Classify this cell by malaria status.
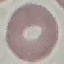

Uninfected.

image type = automatically extracted cell patch, resized to 64 × 64 pixels
stain = Giemsa
capture = smartphone through the microscope eyepiece
preparation = thin smear